Assess this cell for malaria.
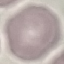

It is uninfected.

{
  "image_type": "cell patch, automatically extracted from a larger field of view and resized to 64 × 64 pixels",
  "capture": "smartphone through the microscope eyepiece",
  "preparation": "thin blood smear",
  "stain": "Giemsa"
}